Identify the parasite.
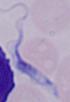
A trypanosome.

Captured at 1000x magnification. Micrograph.